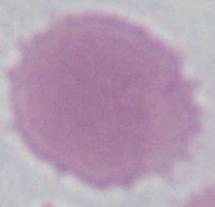
Summary:
  - Modality: micrograph
  - Magnification: 1000x
  - Identification: red blood cell